Name the cell type shown.
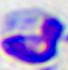

This is a leukocyte.

Captured at 400x magnification. Photomicrograph.